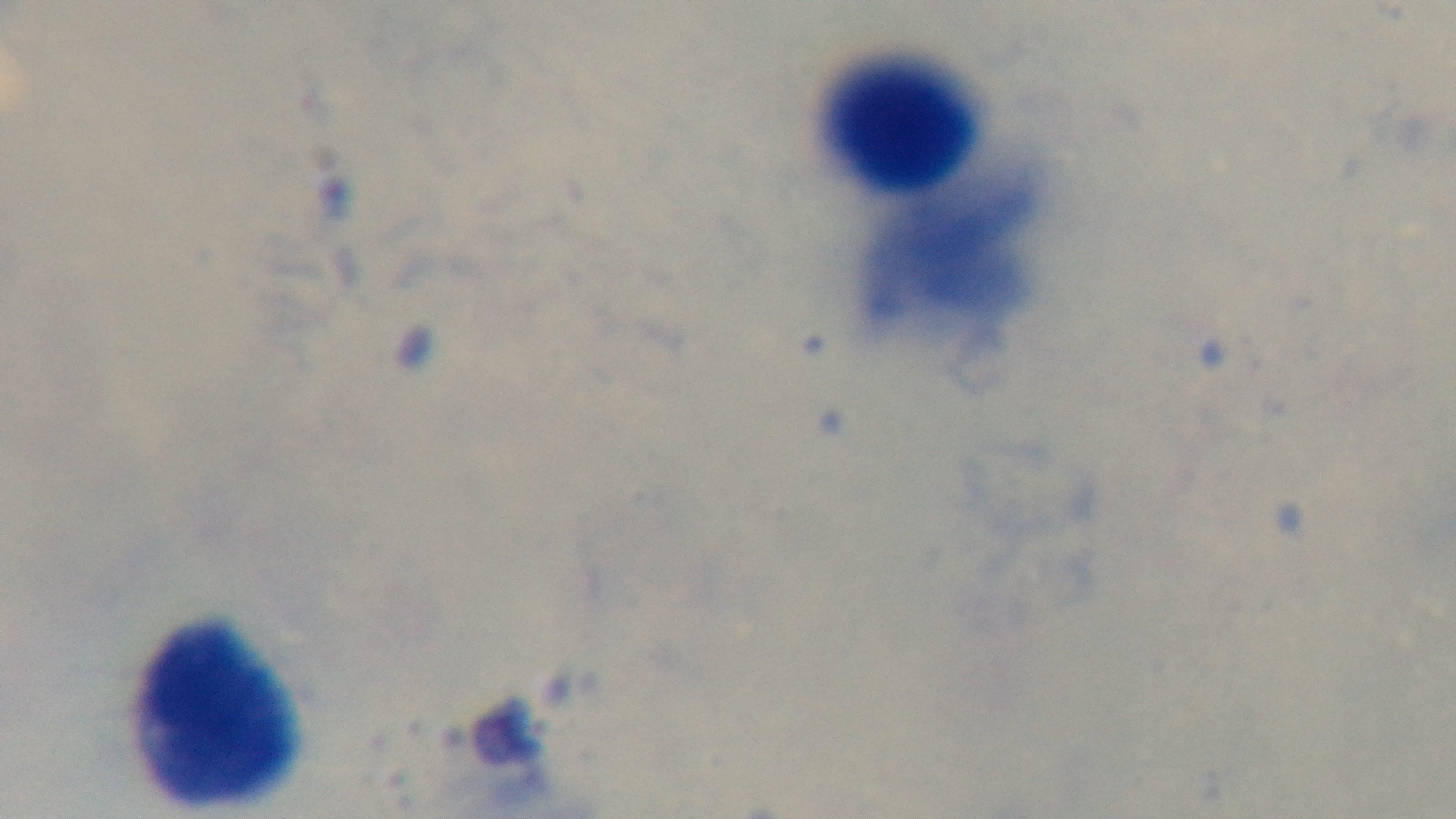
Summary:
  - Field of view: one from the slide
  - Objective: 100x oil immersion
  - Modality: light microscopy
  - Preparation: thick smear
  - Malaria status: negative
  - Capture: mounted 4K digital camera
  - Stain: Giemsa